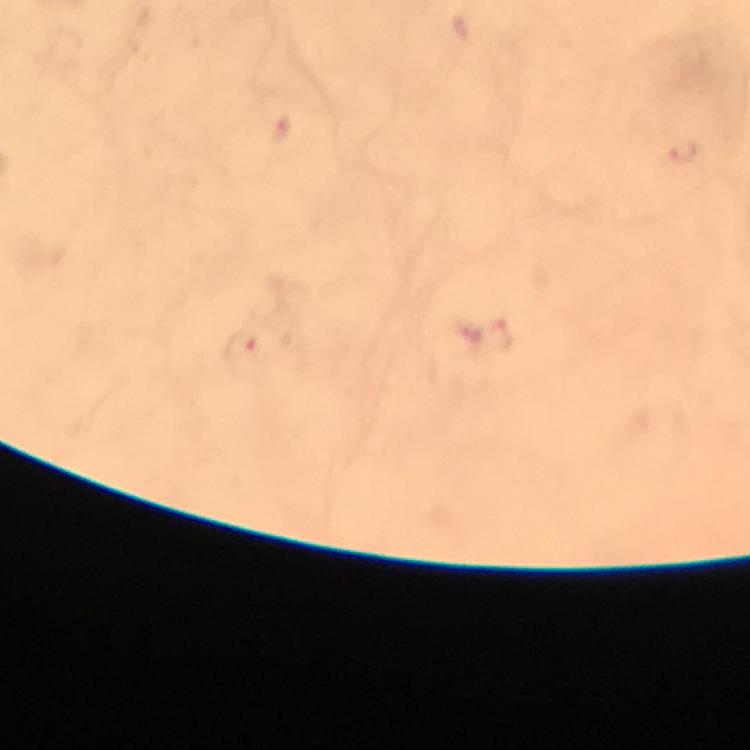

context = from a diagnostic examination for malaria
magnification = 100x
capture = smartphone mounted on the microscope
preparation = thick blood film
stain = Giemsa
immersion oil = applied
image size = 750×750 pixels
cropped from = a single field of view
Plasmodium parasite locations = approximate centers as [x, y] in pixels: [282, 129], [686, 151], [242, 346]